Classify this cell by malaria status.
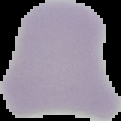
Uninfected.

From a thin blood film. Image is 121×121 pixels. Segmented cell region on a black background.